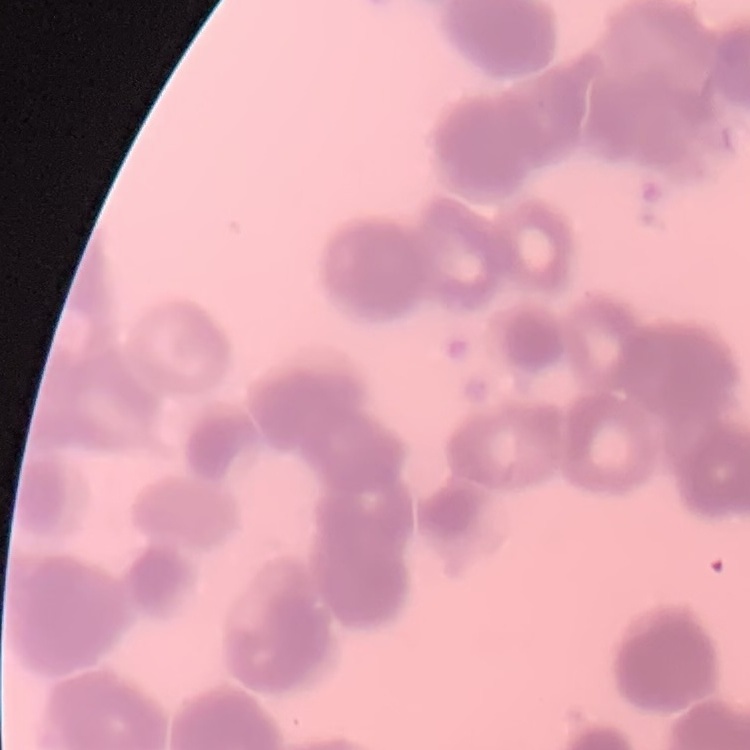
The erythrocytes exhibit rouleaux formation. Thin blood smear. Field's or Giemsa stain. Square crop of a larger photomicrograph.